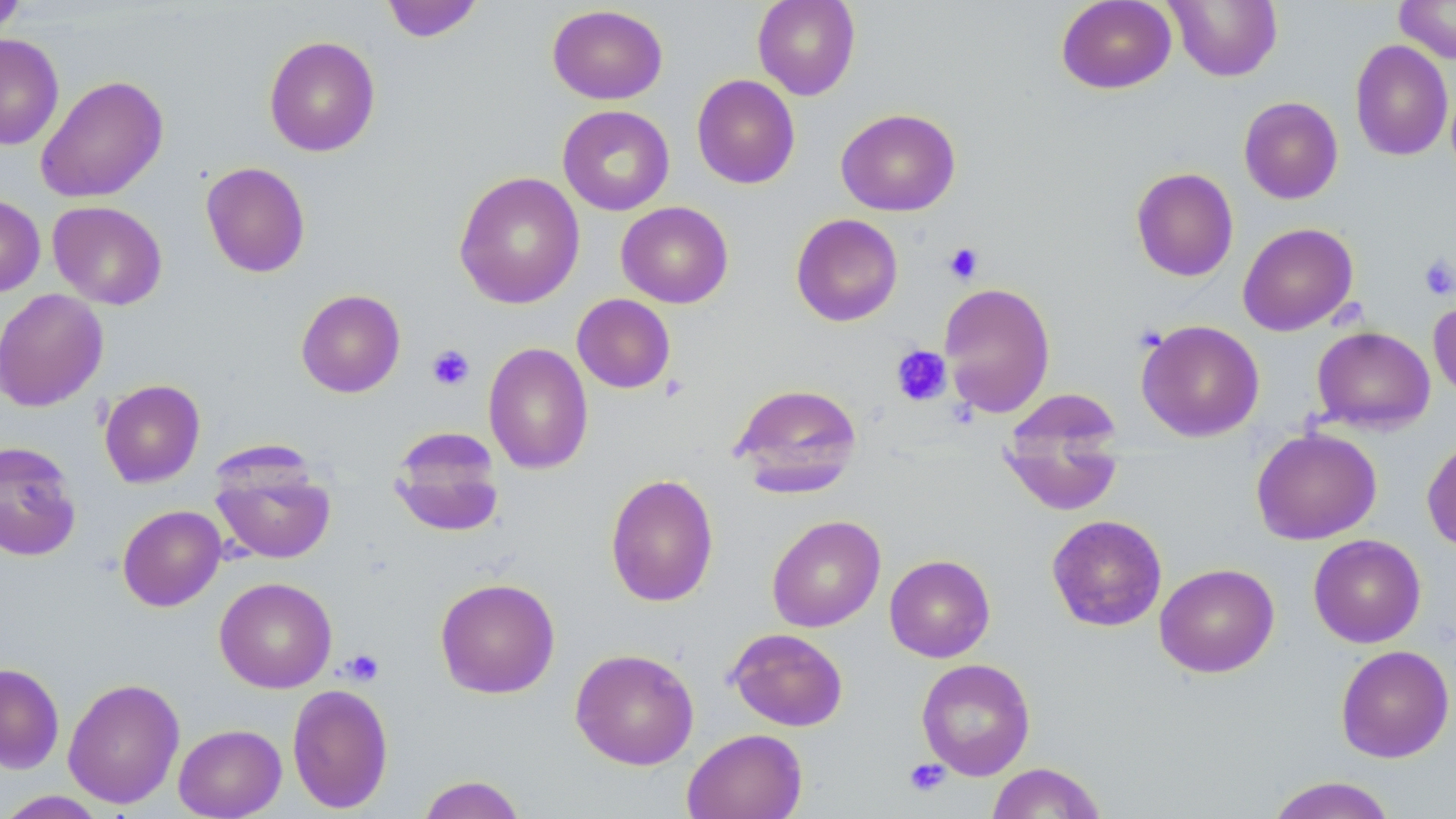

Summary:
  - Coordinate format: approximate bounding boxes as (x1,y1)-(x2,y2) corner pairs in pixels
  - Platelet locations: (943,242)-(985,284), (1418,254)-(1456,300), (427,344)-(475,392), (890,345)-(952,406), (341,648)-(384,686), (904,758)-(951,797)
  - Uninfected red blood cell locations: (0,0)-(26,35), (381,0)-(485,42), (752,0)-(861,100), (1056,0)-(1176,94), (1165,0)-(1282,82), (1394,0)-(1456,64), (547,4)-(668,105), (0,34)-(64,150), (264,35)-(380,157), (1350,40)-(1453,161), (35,74)-(168,203), (691,74)-(800,189), (1238,96)-(1343,204), (558,105)-(674,215), (835,108)-(961,216), (201,162)-(311,278), (1131,167)-(1239,282), (453,171)-(585,309), (0,194)-(45,297), (47,201)-(167,309), (616,201)-(734,308), (790,213)-(903,327), (1238,222)-(1358,336), (938,282)-(1056,418), (0,289)-(108,412), (296,289)-(406,398), (572,293)-(676,394), (1428,298)-(1456,402), (1136,319)-(1265,442), (1311,326)-(1436,433), (483,342)-(593,475), (99,379)-(205,488), (728,382)-(863,496), (999,393)-(1125,517), (388,427)-(505,537), (1251,428)-(1382,545), (1422,435)-(1456,553), (0,441)-(82,562), (210,450)-(337,565), (605,473)-(720,608), (117,505)-(226,611), (766,514)-(886,632), (1046,515)-(1167,632), (1308,534)-(1426,648), (884,554)-(995,662), (1154,562)-(1279,678), (214,576)-(337,693), (434,577)-(560,699), (727,628)-(848,731), (1336,644)-(1454,763), (570,648)-(699,770), (916,658)-(1036,780), (0,663)-(65,774), (62,677)-(185,808), (287,683)-(394,814), (173,724)-(286,818), (682,728)-(808,819), (986,762)-(1107,818), (416,775)-(528,819), (1264,776)-(1399,819), (0,790)-(111,818)
  - Slide-level diagnosis: no evidence of blood parasites
  - Image size: 1456×819 pixels
  - Preparation: thin blood smear
  - Field of view: single
  - Modality: light microscopy
  - Magnification: 1000x
  - Stain: May-Grünwald-Giemsa